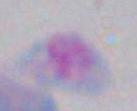
Photomicrograph. Toxoplasma gondii is shown. Captured at 1000x magnification.